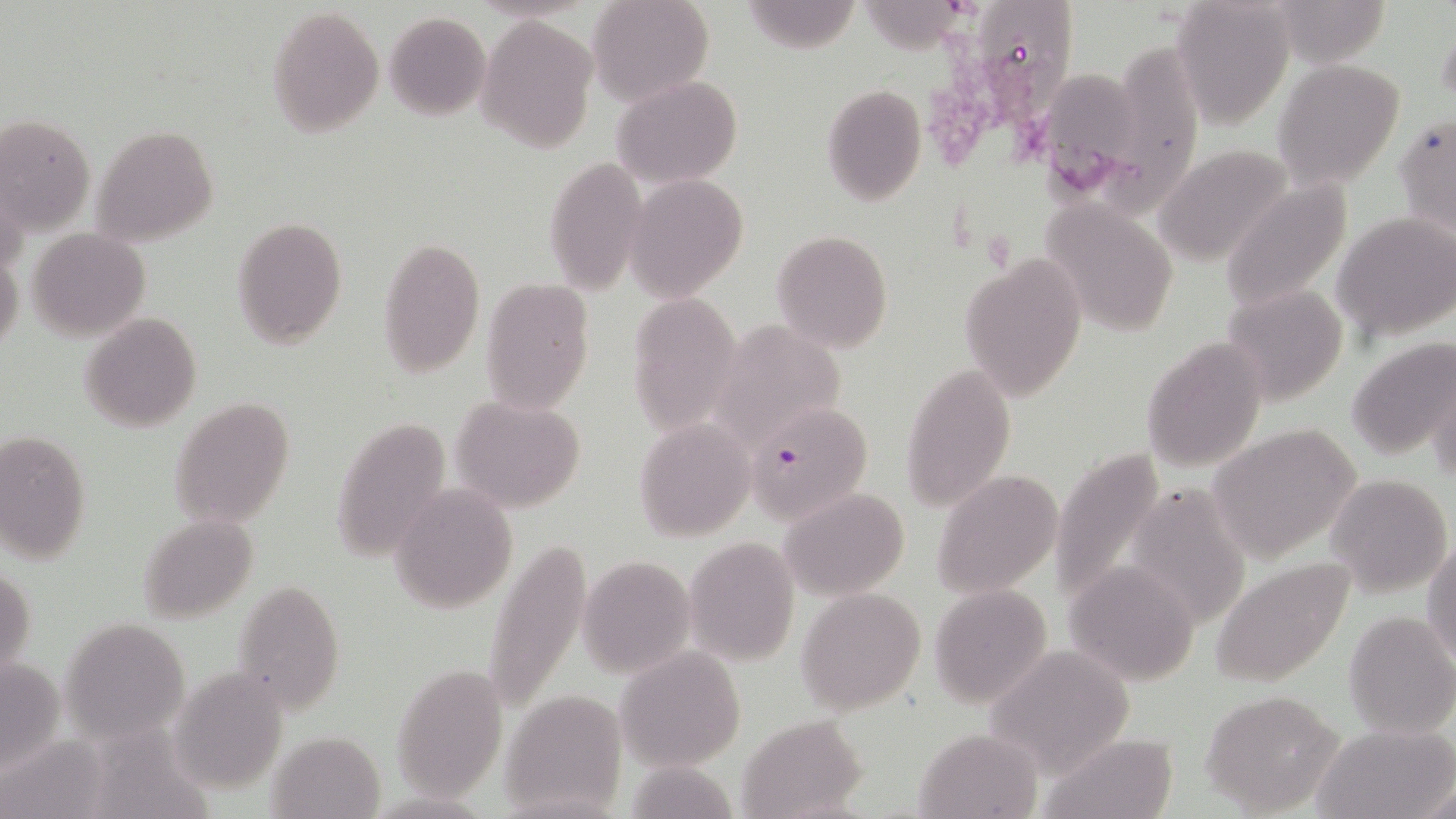

slide-level diagnosis = Plasmodium falciparum
modality = light microscopy
image size = 1456×819 pixels
preparation = thin blood smear
magnification = 1000x
Plasmodium falciparum-infected red blood cell locations = approximate bounding boxes as (x1, y1, x2, y2) in pixels: (748, 398, 872, 521)
stain = May-Grünwald-Giemsa
field of view = single
uninfected red blood cell locations = approximate bounding boxes as (x1, y1, x2, y2) in pixels: (586, 0, 714, 104), (1268, 0, 1392, 67), (740, 1, 861, 53), (865, 1, 973, 54), (985, 1, 1072, 133), (1169, 1, 1295, 129), (266, 4, 384, 139), (383, 11, 490, 120), (478, 14, 598, 155), (1437, 17, 1456, 116), (1103, 36, 1215, 221), (1272, 60, 1403, 189), (1047, 64, 1142, 201), (612, 74, 743, 188), (821, 84, 926, 207), (1394, 113, 1455, 237), (1, 114, 94, 239), (91, 124, 219, 247), (1155, 144, 1295, 267), (544, 156, 646, 295), (624, 176, 748, 299), (1219, 179, 1352, 314), (1042, 200, 1179, 338), (1332, 212, 1456, 341), (230, 216, 349, 350), (25, 228, 151, 341), (771, 231, 893, 353), (375, 238, 484, 376), (0, 249, 23, 357), (960, 252, 1088, 402), (480, 278, 595, 414), (1221, 286, 1348, 406), (625, 292, 741, 435), (78, 312, 202, 433), (709, 320, 847, 452), (1142, 337, 1269, 472), (1345, 337, 1456, 462), (900, 362, 1014, 512), (1427, 367, 1456, 487), (450, 394, 586, 513), (169, 396, 294, 529), (328, 416, 452, 565), (633, 419, 757, 542), (1210, 422, 1361, 564), (0, 429, 92, 563), (1048, 449, 1166, 611), (933, 469, 1061, 599), (1326, 473, 1452, 597), (390, 484, 517, 613), (782, 488, 909, 598), (137, 514, 259, 622), (479, 534, 592, 718), (683, 536, 800, 667), (1422, 537, 1455, 669), (579, 556, 696, 678), (1211, 556, 1357, 689), (1064, 558, 1201, 685), (0, 564, 35, 680), (231, 579, 345, 715), (929, 583, 1052, 710), (796, 587, 926, 715), (1343, 609, 1456, 739), (63, 617, 190, 742), (985, 644, 1138, 775), (618, 649, 745, 772), (391, 661, 507, 799), (167, 668, 289, 792), (1199, 690, 1344, 815), (501, 691, 628, 813), (738, 715, 867, 819), (1312, 723, 1456, 818), (914, 728, 1043, 819), (261, 732, 383, 816), (1036, 733, 1182, 819), (1421, 780, 1455, 817)